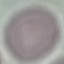
Result: no malaria parasites seen. Automatically extracted cell patch, resized to 64 × 64 pixels. Giemsa-stained preparation. Thin blood smear. Photographed with a smartphone camera at the microscope eyepiece.